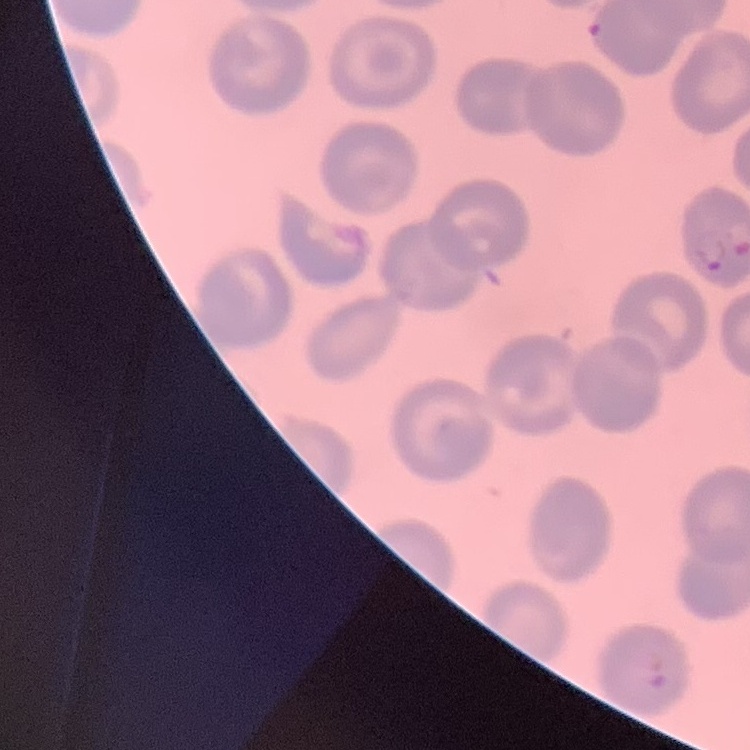
The red blood cells show no rouleaux formation. Square crop of a larger photomicrograph. Thin blood film. Field's or Giemsa stain.